State which parasite is depicted.
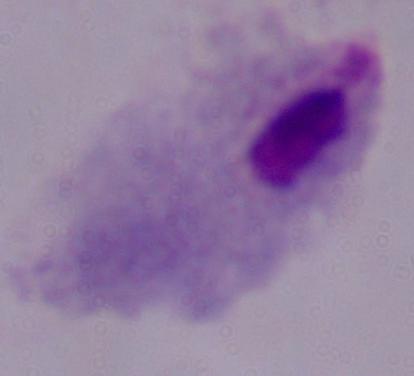
This is a trichomonad.

1000x magnification. Micrograph.